State which parasite is depicted.
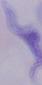

A trypanosome.

{
  "magnification": "1000x",
  "modality": "photomicrograph"
}